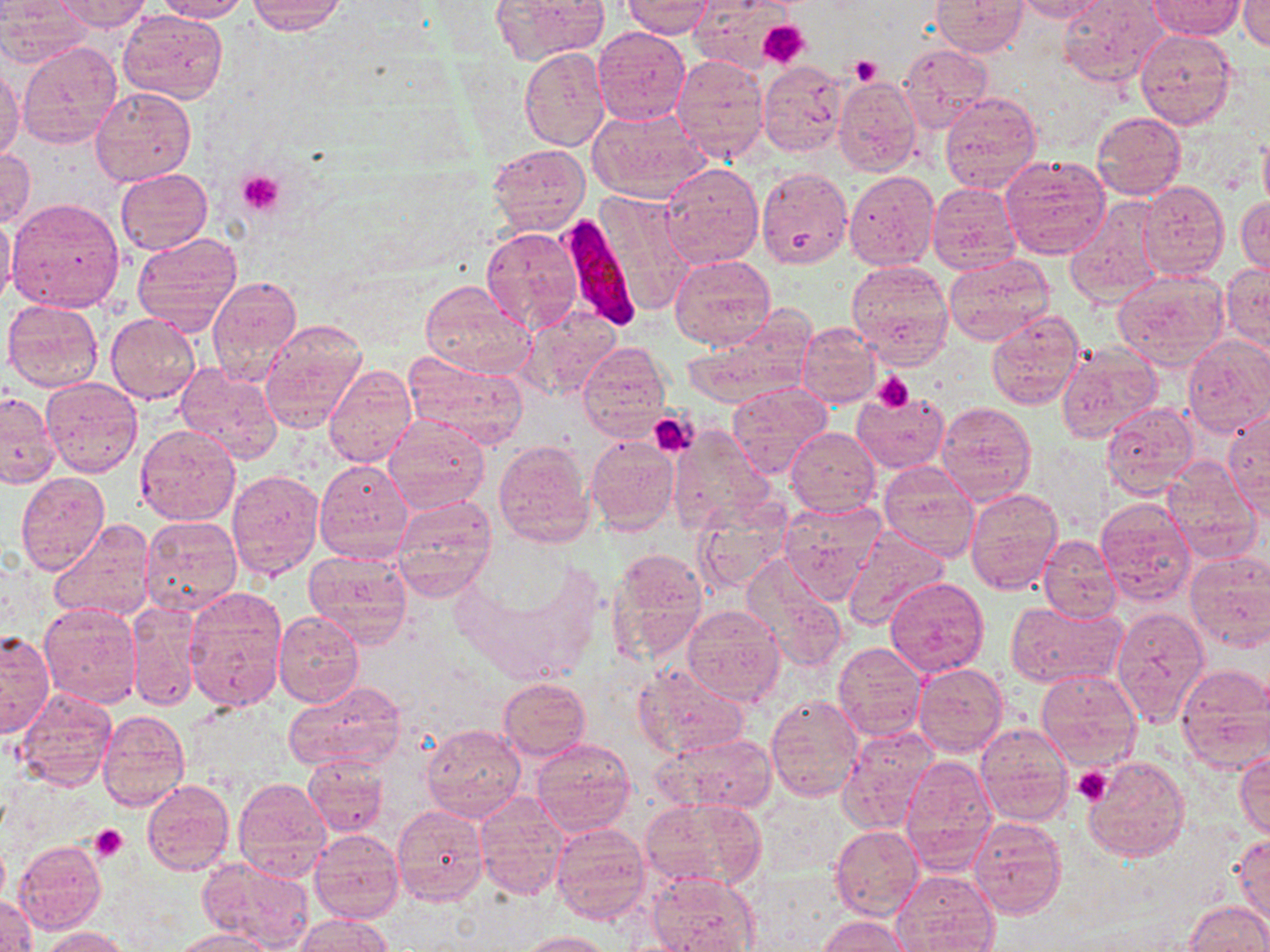
Approximate bounding boxes as named x1/y1/x2/y2 corners in pixels. Platelet locations: (x1=757, y1=19, x2=808, y2=68), (x1=850, y1=54, x2=884, y2=86), (x1=237, y1=169, x2=285, y2=217), (x1=871, y1=372, x2=914, y2=411), (x1=648, y1=410, x2=696, y2=456), (x1=1073, y1=766, x2=1112, y2=806), (x1=89, y1=823, x2=129, y2=861). Uninfected red blood cell locations: (x1=55, y1=0, x2=152, y2=32), (x1=153, y1=0, x2=249, y2=22), (x1=491, y1=0, x2=607, y2=64), (x1=691, y1=0, x2=800, y2=74), (x1=931, y1=0, x2=1027, y2=55), (x1=1013, y1=0, x2=1109, y2=22), (x1=1058, y1=0, x2=1169, y2=87), (x1=248, y1=1, x2=347, y2=35), (x1=621, y1=1, x2=714, y2=37), (x1=1143, y1=1, x2=1241, y2=83), (x1=1239, y1=1, x2=1269, y2=50), (x1=1147, y1=2, x2=1244, y2=39), (x1=0, y1=4, x2=91, y2=67), (x1=118, y1=9, x2=228, y2=105), (x1=2, y1=11, x2=104, y2=118), (x1=592, y1=26, x2=690, y2=125), (x1=1134, y1=29, x2=1236, y2=131), (x1=17, y1=41, x2=123, y2=148), (x1=899, y1=44, x2=990, y2=131), (x1=519, y1=48, x2=610, y2=152), (x1=670, y1=55, x2=768, y2=159), (x1=758, y1=62, x2=846, y2=156), (x1=0, y1=66, x2=23, y2=159), (x1=833, y1=76, x2=921, y2=179), (x1=91, y1=87, x2=196, y2=187), (x1=940, y1=92, x2=1042, y2=193), (x1=588, y1=106, x2=709, y2=203), (x1=1091, y1=111, x2=1186, y2=199), (x1=1258, y1=129, x2=1270, y2=217), (x1=485, y1=144, x2=588, y2=234), (x1=0, y1=148, x2=35, y2=230), (x1=1001, y1=155, x2=1111, y2=261), (x1=659, y1=161, x2=763, y2=269), (x1=756, y1=167, x2=852, y2=269), (x1=117, y1=169, x2=211, y2=253), (x1=844, y1=170, x2=940, y2=271), (x1=1139, y1=181, x2=1229, y2=279), (x1=927, y1=182, x2=1020, y2=275), (x1=596, y1=190, x2=695, y2=315), (x1=1237, y1=195, x2=1270, y2=276), (x1=8, y1=198, x2=126, y2=313), (x1=1063, y1=198, x2=1164, y2=309), (x1=0, y1=212, x2=17, y2=307), (x1=481, y1=226, x2=582, y2=330), (x1=131, y1=233, x2=241, y2=333), (x1=944, y1=254, x2=1054, y2=345), (x1=671, y1=255, x2=776, y2=351), (x1=845, y1=261, x2=953, y2=365), (x1=1220, y1=262, x2=1270, y2=354), (x1=1112, y1=271, x2=1227, y2=370), (x1=209, y1=275, x2=303, y2=383), (x1=420, y1=279, x2=534, y2=378), (x1=2, y1=299, x2=104, y2=393), (x1=517, y1=307, x2=623, y2=403), (x1=986, y1=311, x2=1086, y2=411), (x1=108, y1=313, x2=200, y2=405), (x1=259, y1=319, x2=368, y2=431), (x1=683, y1=319, x2=814, y2=408), (x1=798, y1=325, x2=879, y2=406), (x1=1183, y1=336, x2=1270, y2=437), (x1=1055, y1=341, x2=1161, y2=443), (x1=577, y1=342, x2=671, y2=439), (x1=403, y1=351, x2=528, y2=449), (x1=174, y1=362, x2=282, y2=464), (x1=323, y1=364, x2=417, y2=470), (x1=41, y1=377, x2=143, y2=478), (x1=728, y1=383, x2=831, y2=478), (x1=851, y1=390, x2=948, y2=472), (x1=0, y1=391, x2=59, y2=487), (x1=938, y1=401, x2=1036, y2=506), (x1=1101, y1=402, x2=1199, y2=497), (x1=1224, y1=408, x2=1269, y2=511), (x1=384, y1=414, x2=490, y2=515), (x1=133, y1=422, x2=241, y2=527), (x1=667, y1=425, x2=773, y2=533), (x1=786, y1=427, x2=880, y2=517), (x1=585, y1=435, x2=679, y2=535), (x1=494, y1=439, x2=596, y2=547), (x1=1161, y1=457, x2=1262, y2=563), (x1=315, y1=460, x2=413, y2=563), (x1=879, y1=462, x2=980, y2=561), (x1=226, y1=469, x2=322, y2=579), (x1=16, y1=472, x2=110, y2=574), (x1=963, y1=488, x2=1063, y2=597), (x1=391, y1=494, x2=496, y2=601), (x1=777, y1=498, x2=885, y2=600), (x1=1096, y1=500, x2=1197, y2=606), (x1=691, y1=504, x2=793, y2=593), (x1=139, y1=516, x2=242, y2=616), (x1=48, y1=519, x2=156, y2=623), (x1=840, y1=527, x2=950, y2=631), (x1=1037, y1=532, x2=1121, y2=624), (x1=608, y1=547, x2=707, y2=661), (x1=303, y1=549, x2=413, y2=646), (x1=1184, y1=553, x2=1270, y2=652), (x1=738, y1=555, x2=848, y2=672), (x1=885, y1=577, x2=990, y2=678), (x1=184, y1=592, x2=286, y2=712), (x1=1008, y1=601, x2=1127, y2=689), (x1=38, y1=602, x2=142, y2=708), (x1=127, y1=604, x2=200, y2=712), (x1=680, y1=605, x2=786, y2=706), (x1=1111, y1=607, x2=1208, y2=725), (x1=274, y1=610, x2=365, y2=707), (x1=0, y1=631, x2=55, y2=737), (x1=832, y1=641, x2=927, y2=741), (x1=633, y1=663, x2=750, y2=758), (x1=913, y1=663, x2=1008, y2=756), (x1=1176, y1=663, x2=1270, y2=773), (x1=1036, y1=668, x2=1142, y2=770), (x1=498, y1=677, x2=590, y2=761), (x1=281, y1=681, x2=407, y2=776), (x1=15, y1=688, x2=116, y2=792), (x1=766, y1=695, x2=863, y2=802), (x1=97, y1=710, x2=189, y2=811), (x1=975, y1=722, x2=1073, y2=825), (x1=420, y1=723, x2=524, y2=822), (x1=838, y1=727, x2=938, y2=832), (x1=657, y1=733, x2=778, y2=815), (x1=531, y1=738, x2=635, y2=837), (x1=1235, y1=750, x2=1270, y2=840), (x1=1084, y1=754, x2=1190, y2=861), (x1=898, y1=755, x2=998, y2=873), (x1=304, y1=757, x2=388, y2=836), (x1=232, y1=777, x2=331, y2=883), (x1=142, y1=780, x2=234, y2=877), (x1=473, y1=792, x2=569, y2=901), (x1=643, y1=797, x2=766, y2=891), (x1=392, y1=806, x2=487, y2=905), (x1=969, y1=816, x2=1067, y2=919), (x1=549, y1=823, x2=649, y2=924), (x1=832, y1=825, x2=924, y2=920), (x1=310, y1=830, x2=403, y2=923), (x1=1231, y1=832, x2=1270, y2=929), (x1=14, y1=839, x2=105, y2=933), (x1=0, y1=840, x2=9, y2=907), (x1=196, y1=856, x2=313, y2=952), (x1=891, y1=870, x2=999, y2=951), (x1=646, y1=873, x2=761, y2=951), (x1=1, y1=892, x2=36, y2=952), (x1=1186, y1=901, x2=1270, y2=951), (x1=296, y1=914, x2=394, y2=952), (x1=819, y1=916, x2=912, y2=952), (x1=40, y1=926, x2=135, y2=952), (x1=177, y1=930, x2=275, y2=952), (x1=516, y1=930, x2=615, y2=951). Plasmodium falciparum-infected red blood cell locations: (x1=554, y1=214, x2=640, y2=331). Slide-level diagnosis: Plasmodium falciparum. Optical microscopy. Image is 1270×952 pixels. 1000x magnification. Thin blood film. May-Grünwald-Giemsa stain. One field of a larger specimen.